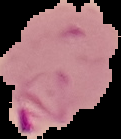
image size = 121×139 pixels
result = malaria parasites identified
image type = segmented cell region on a black background
preparation = thin blood smear